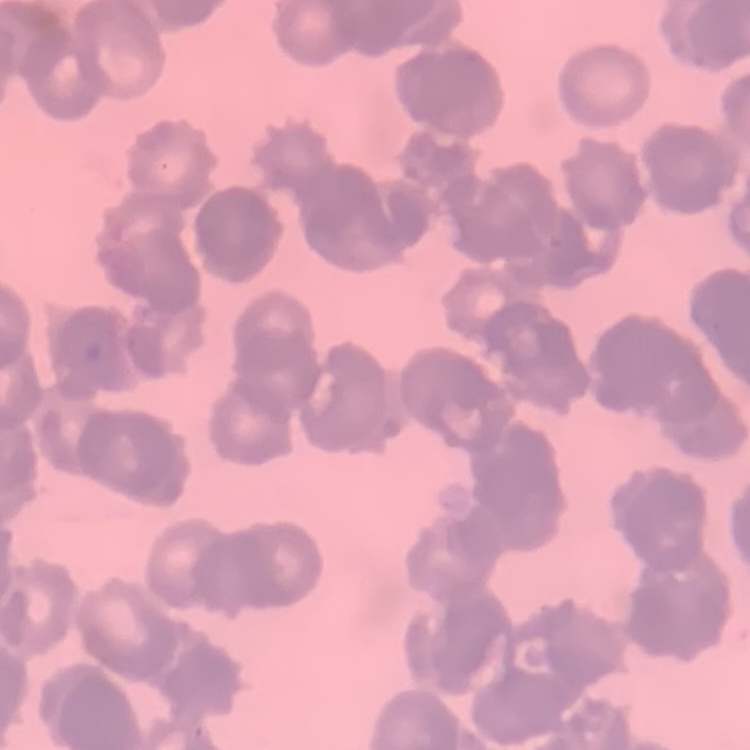

The erythrocytes exhibit rouleaux formation. Square crop of a larger photomicrograph. Field's or Giemsa stain. Thin peripheral smear.